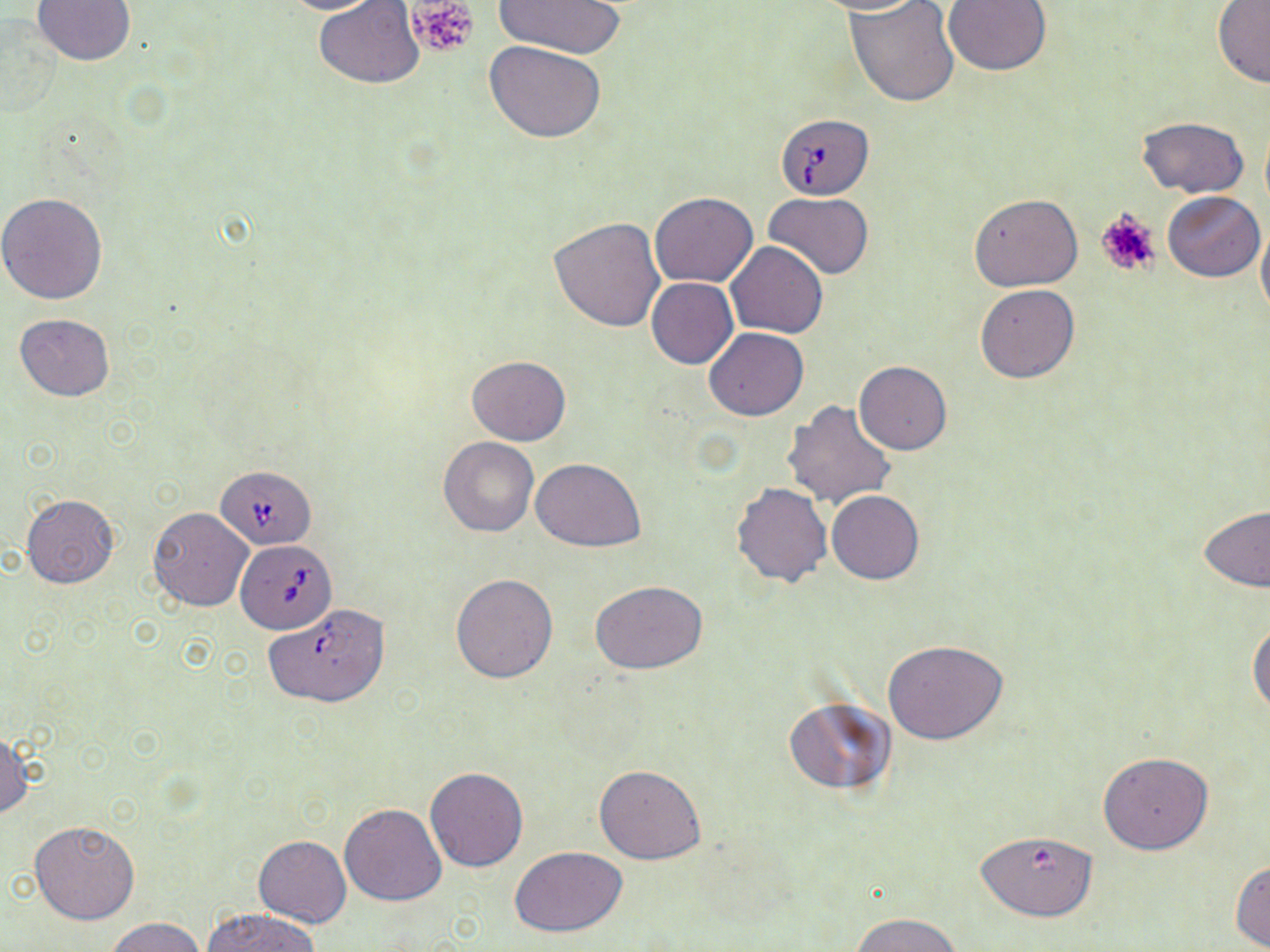 Approximate bounding boxes as (x1,y1)-(x2,y2) corner pairs in pixels. Uninfected red blood cell locations: (32,0)-(135,67), (270,0)-(387,15), (492,0)-(628,58), (806,0)-(927,16), (846,0)-(960,106), (943,0)-(1051,75), (313,1)-(425,87), (1213,1)-(1270,88), (485,41)-(607,141), (1137,116)-(1248,198), (1163,190)-(1264,281), (0,192)-(108,305), (650,192)-(757,287), (764,193)-(874,278), (970,193)-(1082,290), (1256,215)-(1270,322), (549,216)-(666,333), (726,242)-(829,337), (646,277)-(738,368), (975,285)-(1080,383), (13,314)-(115,401), (705,328)-(808,420), (466,356)-(571,445), (854,361)-(952,455), (783,399)-(897,508), (438,437)-(538,537), (532,457)-(645,551), (731,481)-(833,587), (827,489)-(924,583), (22,495)-(119,589), (1199,505)-(1270,591), (148,507)-(253,612), (450,573)-(558,684), (592,582)-(706,675), (1248,615)-(1270,719), (883,641)-(1008,745), (784,698)-(894,795), (0,729)-(33,821), (1098,751)-(1212,855), (595,765)-(707,864), (424,768)-(529,872), (339,803)-(446,906), (28,820)-(139,925), (975,827)-(1099,922), (253,836)-(352,928), (509,846)-(629,936), (1230,860)-(1270,950), (203,908)-(320,952), (853,913)-(963,952), (104,916)-(206,952). Platelet locations: (406,0)-(479,60), (1093,207)-(1162,278). Babesia divergens-infected red blood cell locations: (774,113)-(874,198), (218,465)-(318,548), (234,541)-(336,633), (263,603)-(390,707). Slide-level diagnosis: Babesia divergens. Light microscopy. Captured at 1000x magnification. One field of a larger specimen. Thin blood smear. May-Grünwald-Giemsa stain. Image is 1270×952 pixels.